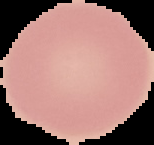

{
  "image_size": "154×145 pixels",
  "malaria_status": "uninfected",
  "preparation": "thin blood smear",
  "image_type": "segmented cell region with the area outside set to black"
}